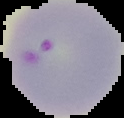
malaria_status: parasitized
preparation: thin blood film
image_size: 124×118 pixels
image_type: segmented cell region on a black background